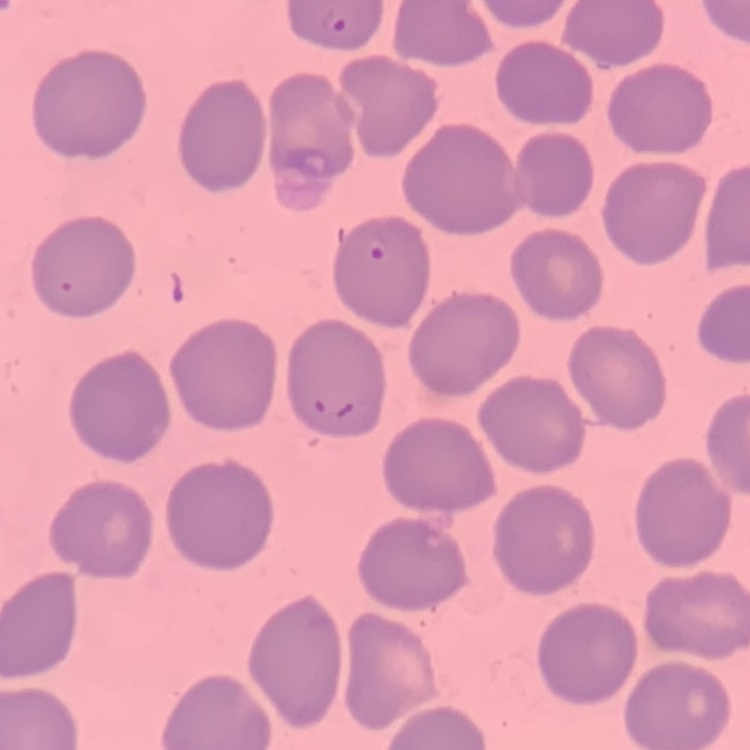

Summary:
  - Red blood cell morphology: no rouleaux formation
  - Stain: Field's or Giemsa
  - Image type: square crop of a larger photomicrograph
  - Preparation: thin blood film